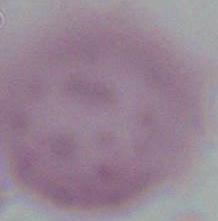

{
  "magnification": "1000x",
  "modality": "photomicrograph",
  "identification": "red blood cell"
}